State the preparation type.
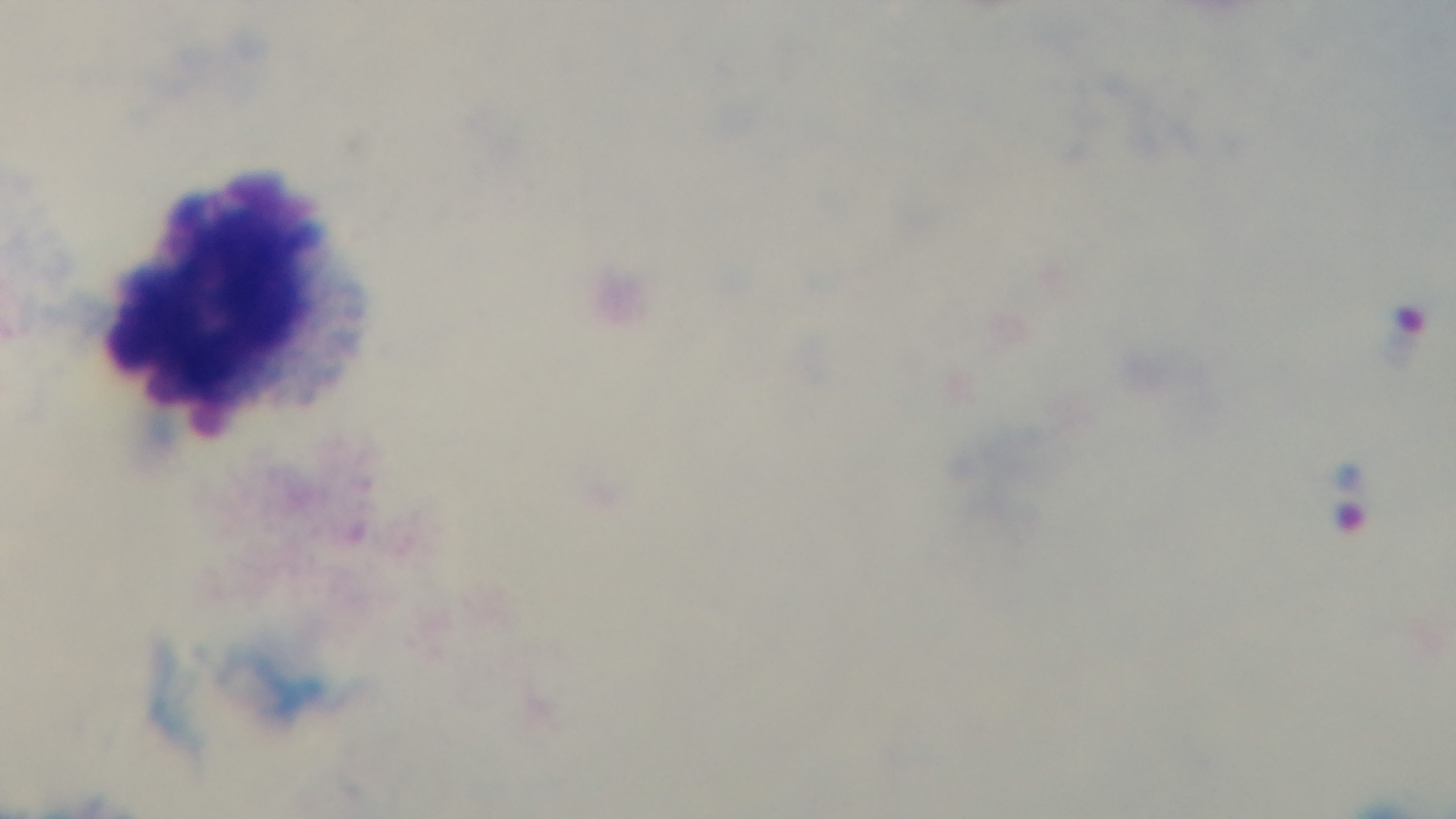
Thick.

{
  "objective": "100x oil immersion",
  "capture": "mounted 4K digital camera",
  "stain": "Giemsa",
  "malaria_status": "infected",
  "field_of_view": "one from the slide",
  "modality": "light microscopy"
}